Classify this cell by malaria status.
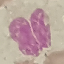
It is uninfected.

{
  "image_type": "cell patch, automatically extracted from a larger field of view and resized to 64 × 64 pixels",
  "preparation": "thin smear",
  "capture": "smartphone through the microscope eyepiece",
  "stain": "Giemsa"
}